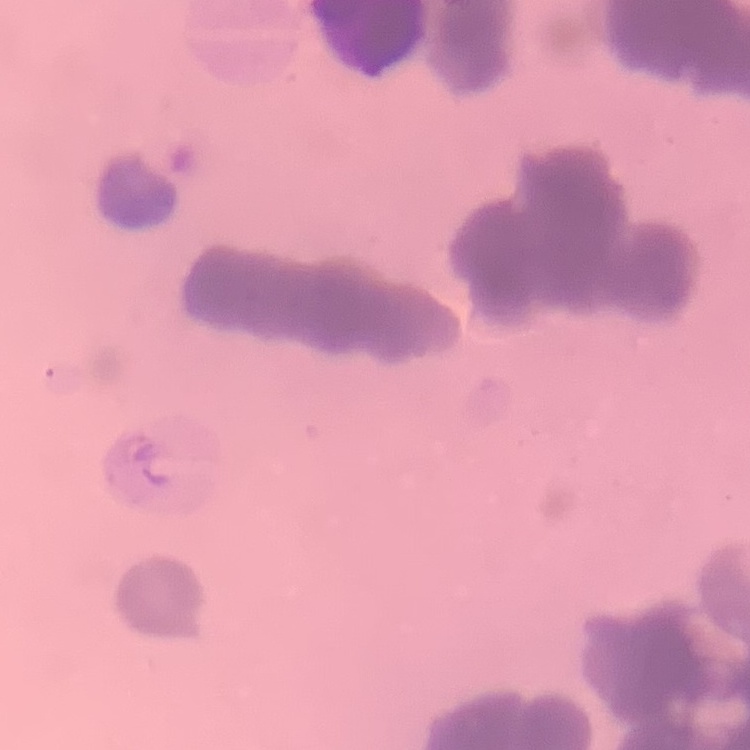

Summary:
  - Red blood cell morphology: rouleaux formation
  - Stain: Field's or Giemsa
  - Preparation: thin peripheral smear
  - Image type: square crop of a larger photomicrograph